Describe the morphology of the erythrocytes.
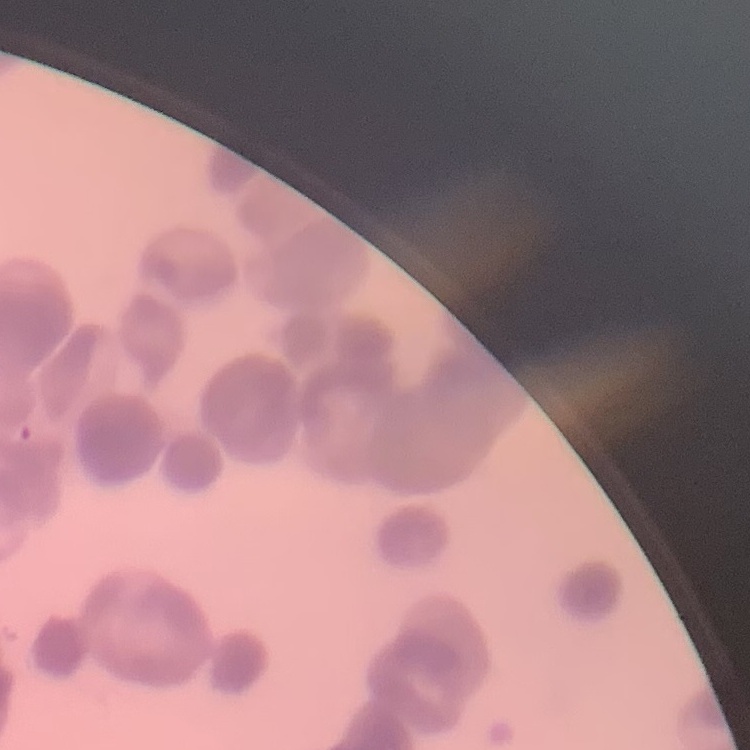
They show rouleaux formation.

stain = Field's or Giemsa
image type = one tile cut from a larger photomicrograph
preparation = thin blood film